Identify the parasite.
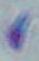
This is Toxoplasma gondii.

Summary:
  - Magnification: 1000x
  - Modality: micrograph